Comment on the morphology of the erythrocytes.
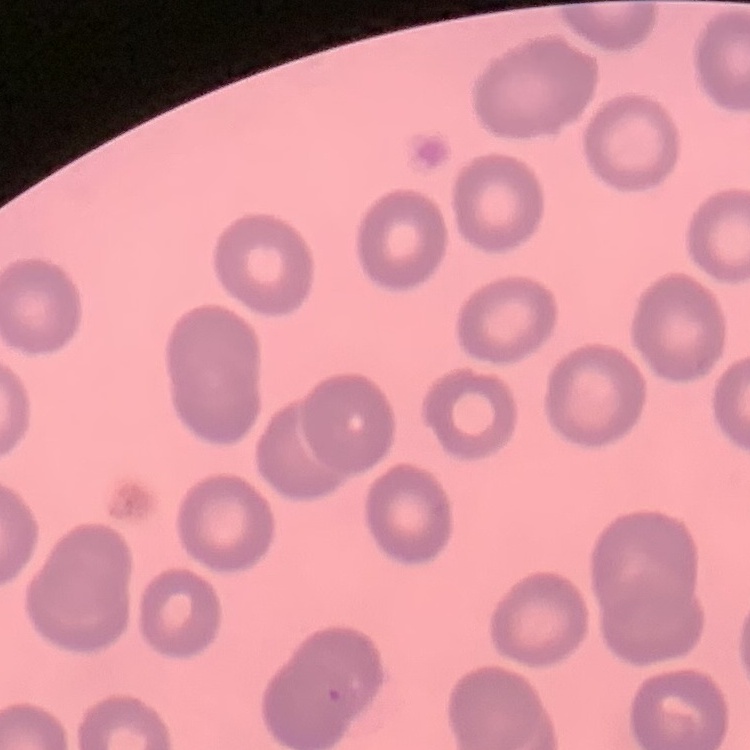
They show no rouleaux formation.

Thin peripheral smear. One tile cut from a larger photomicrograph. Stained with either Field's or Giemsa.